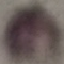
Summary:
  - Result: no malaria parasites seen
  - Capture: smartphone camera at the microscope eyepiece
  - Image type: cell patch, automatically extracted from a larger field of view and resized to 64 × 64 pixels
  - Preparation: thin blood smear
  - Stain: Giemsa